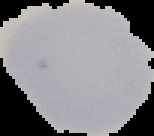
Summary:
  - Image type: cell region segmented out of the field of view; surrounding area masked to black
  - Image size: 154×136 pixels
  - Preparation: thin blood film
  - Result: no malaria parasites seen